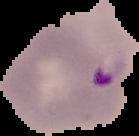

preparation = thin blood film
image size = 139×136 pixels
malaria status = parasitized
image type = segmented cell region on a black background